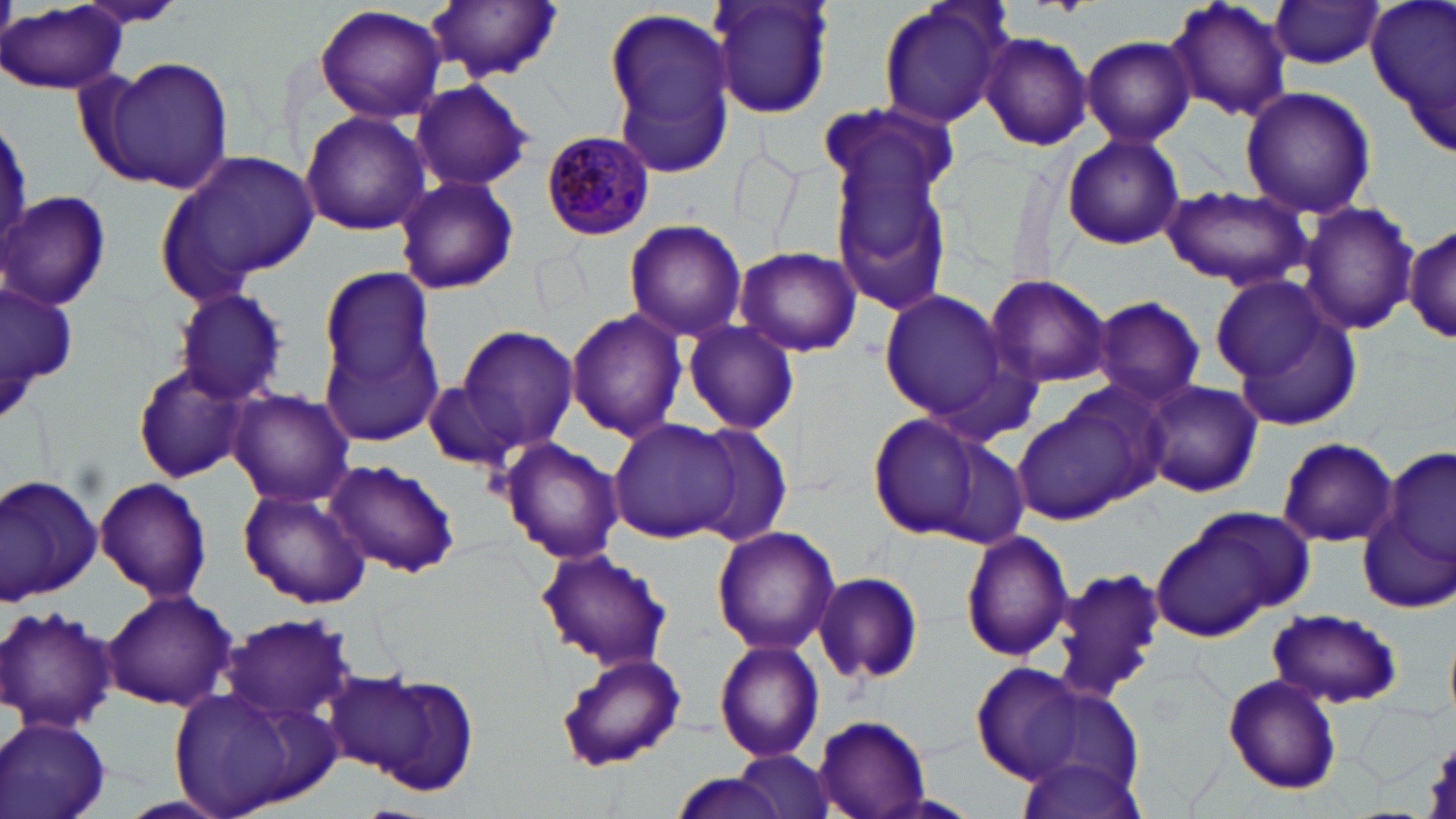
slide-level diagnosis = Plasmodium malariae
preparation = thin blood film
modality = optical microscopy
image size = 1456×819 pixels
magnification = 1000x
Plasmodium malariae-infected red blood cell locations = approximate bounding boxes as (x1,y1)-(x2,y2) corner pairs in pixels: (540,129)-(655,241)
field of view = one of a larger specimen
uninfected red blood cell locations = approximate bounding boxes as (x1,y1)-(x2,y2) corner pairs in pixels: (69,0)-(193,32), (427,0)-(562,81), (705,0)-(837,121), (876,0)-(1016,131), (1166,0)-(1291,122), (1268,0)-(1387,69), (1364,1)-(1456,160), (602,3)-(739,171), (1,4)-(127,95), (314,4)-(448,124), (979,31)-(1093,150), (1080,35)-(1195,146), (95,59)-(234,193), (409,78)-(535,193), (1238,86)-(1376,218), (300,110)-(430,237), (0,113)-(30,259), (825,118)-(959,319), (1061,133)-(1184,251), (159,149)-(316,296), (393,173)-(520,296), (1160,186)-(1311,292), (0,190)-(112,310), (1299,202)-(1418,336), (622,218)-(747,341), (1404,220)-(1454,347), (732,245)-(864,357), (316,261)-(440,407), (983,273)-(1113,389), (1209,273)-(1335,387), (1,275)-(78,426), (168,286)-(291,406), (877,288)-(1019,427), (1092,296)-(1206,406), (1224,302)-(1363,429), (564,306)-(688,443), (317,319)-(446,453), (680,320)-(800,435), (451,324)-(580,459), (132,364)-(251,484), (423,367)-(538,475), (1142,381)-(1264,499), (227,391)-(360,507), (1010,395)-(1155,527), (864,412)-(992,541), (609,419)-(737,543), (688,425)-(795,548), (1276,437)-(1399,548), (500,438)-(625,564), (1383,445)-(1456,569), (325,459)-(460,578), (0,474)-(101,605), (93,478)-(212,604), (238,487)-(371,609), (1150,509)-(1306,642), (1359,510)-(1455,615), (711,525)-(841,655), (960,530)-(1075,662), (535,548)-(672,672), (1052,565)-(1166,702), (813,570)-(924,685), (102,589)-(235,711), (0,604)-(118,733), (1267,608)-(1404,707), (216,613)-(363,730), (714,639)-(826,765), (554,650)-(687,771), (974,663)-(1087,780), (334,669)-(480,794), (1222,674)-(1343,795), (167,684)-(332,819), (0,715)-(113,819), (814,715)-(930,819), (1012,750)-(1149,819), (733,751)-(838,819), (668,771)-(791,819)
stain = May-Grünwald-Giemsa